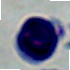

Summary:
  - Magnification: 1000x
  - Modality: micrograph
  - Identification: leukocyte